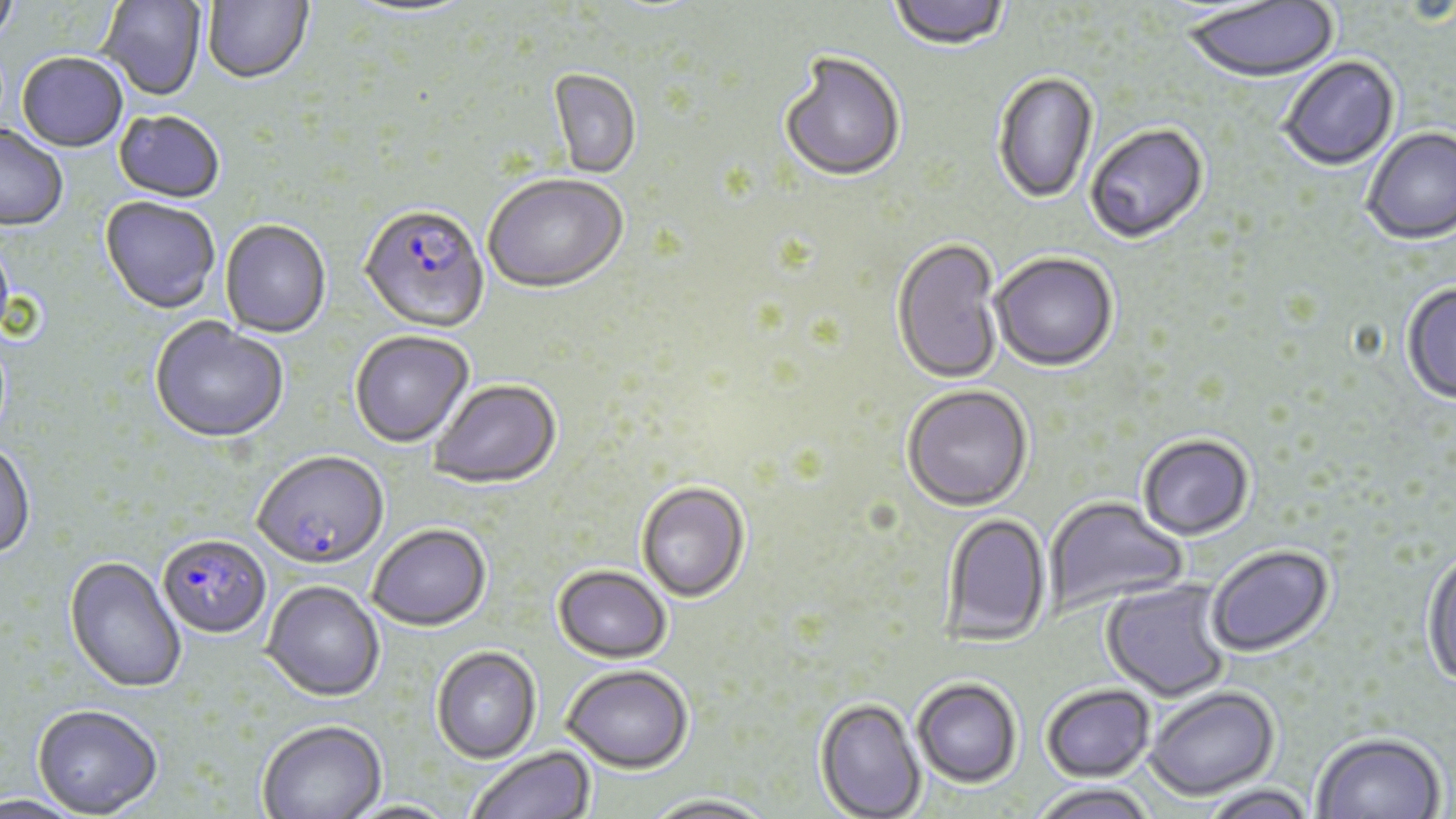
slide-level diagnosis = Plasmodium falciparum
field of view = one of a larger specimen
Plasmodium falciparum-infected red blood cell locations = approximate bounding boxes as (x1,y1)-(x2,y2) corner pairs in pixels: (359,208)-(490,335), (254,454)-(390,573), (158,536)-(272,641)
stain = May-Grünwald-Giemsa
uninfected red blood cell locations = approximate bounding boxes as (x1,y1)-(x2,y2) corner pairs in pixels: (0,0)-(20,52), (97,0)-(207,103), (202,0)-(314,87), (888,0)-(1011,53), (1181,0)-(1339,87), (343,1)-(478,21), (16,54)-(128,154), (779,55)-(906,184), (1279,57)-(1401,172), (548,70)-(641,180), (993,73)-(1099,206), (114,112)-(224,205), (1085,126)-(1209,246), (0,128)-(68,232), (1362,128)-(1456,247), (483,176)-(629,297), (99,198)-(219,315), (220,222)-(331,339), (891,240)-(1004,386), (990,254)-(1118,374), (1401,283)-(1456,406), (149,319)-(288,446), (350,332)-(474,450), (429,381)-(563,490), (902,387)-(1033,513), (1138,435)-(1254,542), (0,444)-(35,562), (636,483)-(750,604), (1043,496)-(1188,613), (940,512)-(1051,646), (368,527)-(492,634), (1206,545)-(1335,657), (1421,547)-(1456,691), (64,558)-(186,695), (552,567)-(672,666), (1101,578)-(1233,703), (261,583)-(385,704), (431,648)-(541,765), (562,668)-(693,776), (912,680)-(1022,790), (1041,685)-(1155,783), (1144,687)-(1280,802), (813,699)-(926,819), (32,707)-(163,819), (259,722)-(386,819), (1311,733)-(1446,818), (468,748)-(595,819), (1030,784)-(1157,819), (1198,785)-(1318,819), (0,795)-(88,819), (643,797)-(778,819), (340,800)-(465,818)
magnification = 1000x
image size = 1456×819 pixels
modality = optical microscopy
preparation = thin blood smear